Give the extent of all uninfected red blood cells.
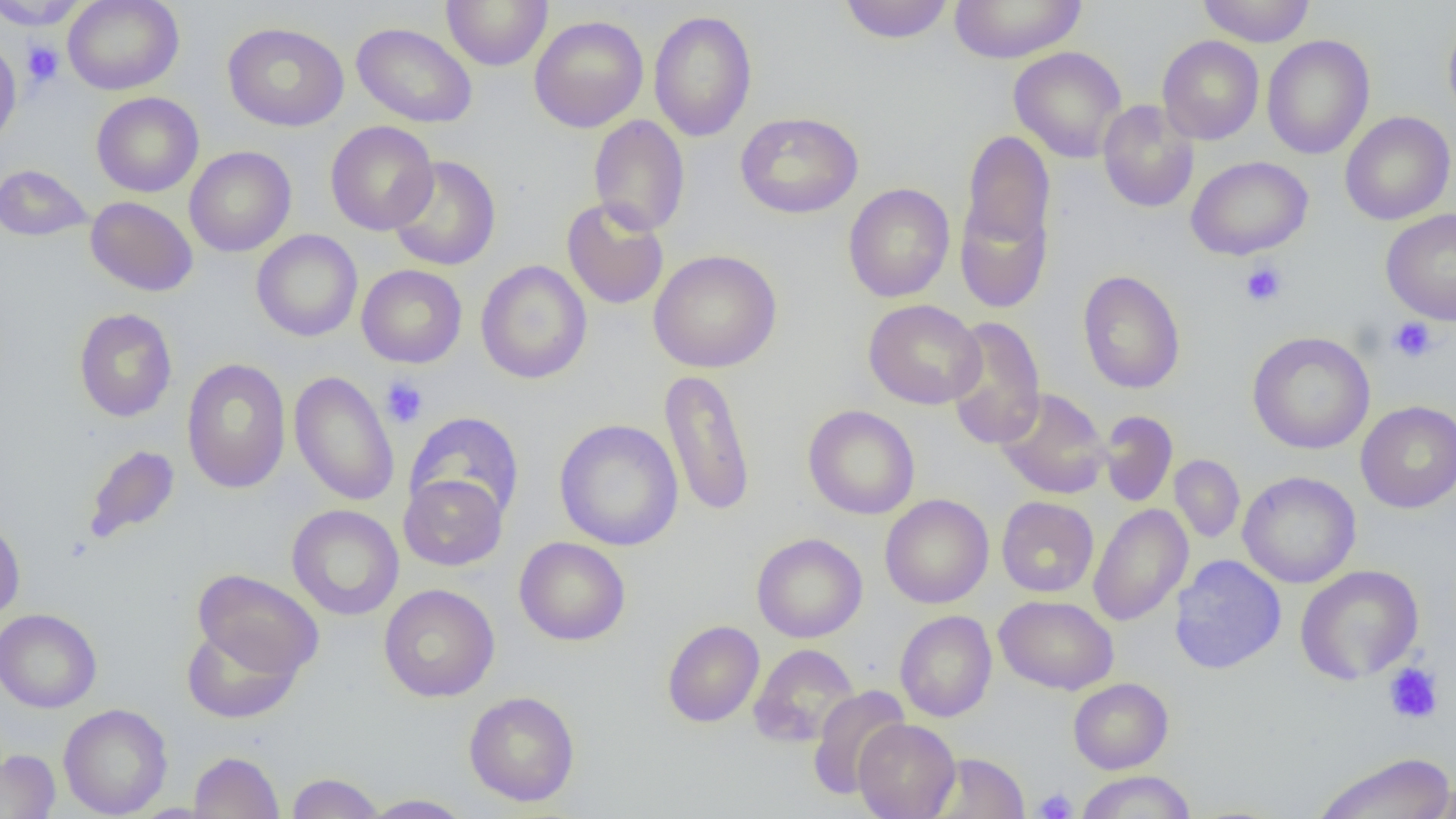
Approximate bounding boxes as (x1,y1)-(x2,y2) corner pairs in pixels.
Uninfected red blood cells: (62,0)-(184,95), (442,0)-(552,71), (839,0)-(955,44), (948,0)-(1087,64), (1198,0)-(1315,47), (0,1)-(88,30), (648,10)-(757,142), (530,15)-(649,133), (1443,17)-(1456,124), (223,21)-(349,132), (351,22)-(478,128), (1262,35)-(1375,160), (1157,36)-(1264,145), (0,39)-(22,149), (1009,46)-(1127,163), (91,92)-(204,197), (1097,100)-(1200,213), (735,111)-(863,219), (1340,111)-(1455,225), (588,115)-(690,237), (324,121)-(438,236), (961,129)-(1055,258), (184,147)-(296,256), (387,155)-(501,271), (1186,156)-(1313,260), (0,164)-(92,241), (843,183)-(955,303), (86,197)-(198,296), (955,197)-(1054,314), (562,198)-(669,310), (1381,207)-(1456,325), (251,230)-(363,342), (648,249)-(782,373), (476,260)-(592,384), (356,264)-(467,368), (1077,270)-(1186,395), (864,299)-(985,409), (74,307)-(177,422), (944,316)-(1046,450), (1247,331)-(1375,454), (181,358)-(291,494), (659,367)-(756,518), (289,370)-(399,506), (994,387)-(1110,499), (1356,401)-(1456,513), (803,405)-(920,520), (404,411)-(525,524), (1098,411)-(1178,508), (554,419)-(684,551), (82,444)-(181,545), (1169,455)-(1245,543), (1237,471)-(1361,588), (399,473)-(508,571), (880,494)-(994,609), (997,496)-(1099,597), (1088,503)-(1193,626), (286,504)-(404,620), (0,515)-(26,623), (752,533)-(867,642), (514,537)-(630,646), (1169,554)-(1286,674), (1295,564)-(1424,684), (192,568)-(324,679), (378,584)-(500,702), (994,595)-(1119,695), (0,608)-(102,712), (895,611)-(997,722), (662,620)-(764,727), (181,624)-(302,724), (748,643)-(859,748), (1068,678)-(1173,773), (807,685)-(911,800), (463,691)-(580,807), (58,703)-(173,818), (853,718)-(960,819), (0,749)-(61,818), (188,751)-(285,818), (1313,751)-(1455,819), (930,753)-(1029,818), (1075,770)-(1196,819), (287,773)-(384,818), (1420,780)-(1456,819), (360,794)-(475,818).

Summary:
  - Platelet locations: (22,41)-(64,87), (1240,261)-(1287,307), (1388,317)-(1438,363), (381,377)-(429,428), (1383,662)-(1443,724), (1033,787)-(1078,818)
  - Slide-level diagnosis: no evidence of blood parasites
  - Magnification: 1000x
  - Modality: light microscopy
  - Field of view: one of a larger specimen
  - Preparation: thin blood smear
  - Image size: 1456×819 pixels